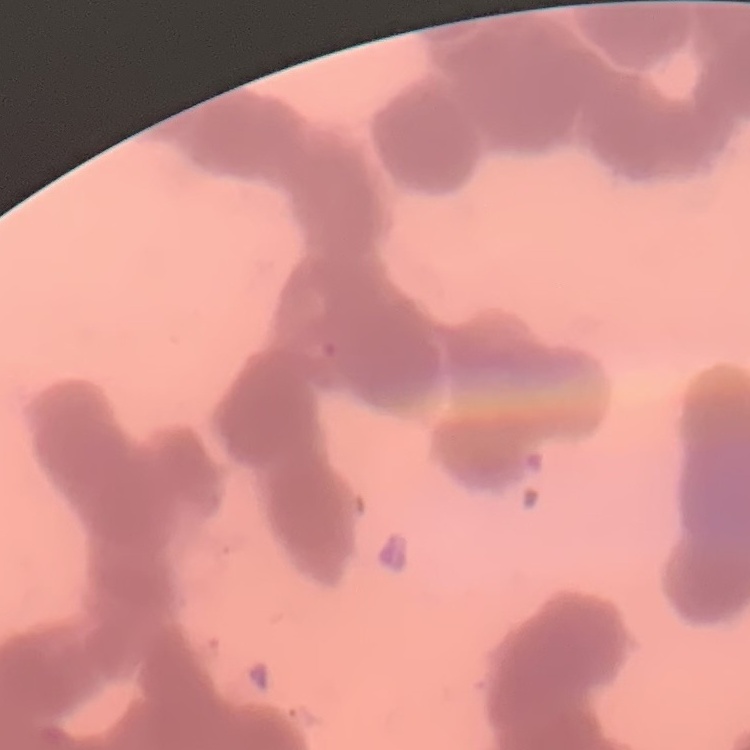

Summary:
  - Red blood cell morphology: rouleaux formation
  - Preparation: thin peripheral smear
  - Image type: one tile cut from a larger photomicrograph
  - Stain: Field's or Giemsa